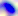
{
  "magnification": "400x",
  "modality": "photomicrograph",
  "identification": "Toxoplasma gondii"
}